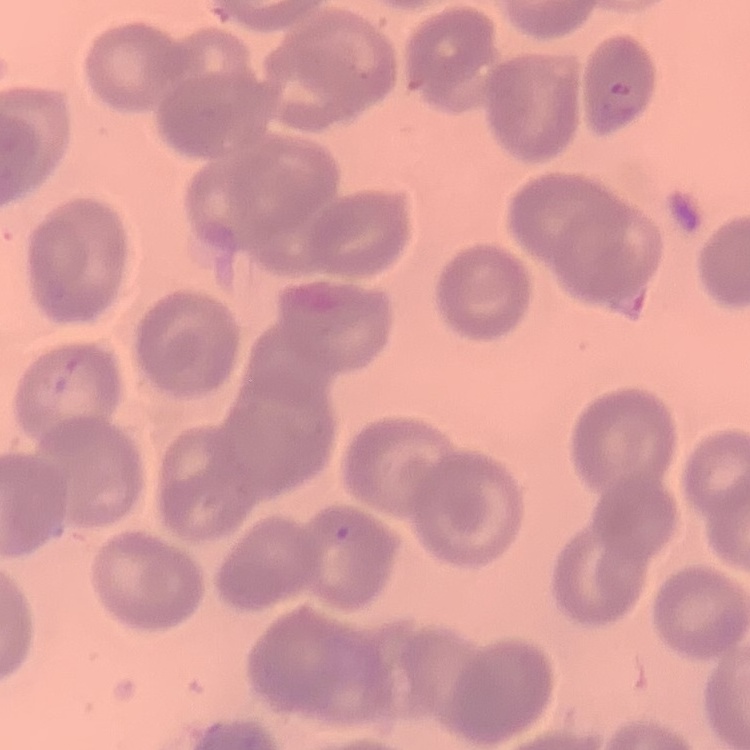

red blood cell morphology = no rouleaux formation
preparation = thin blood film
image type = one tile cut from a larger photomicrograph
stain = Field's or Giemsa